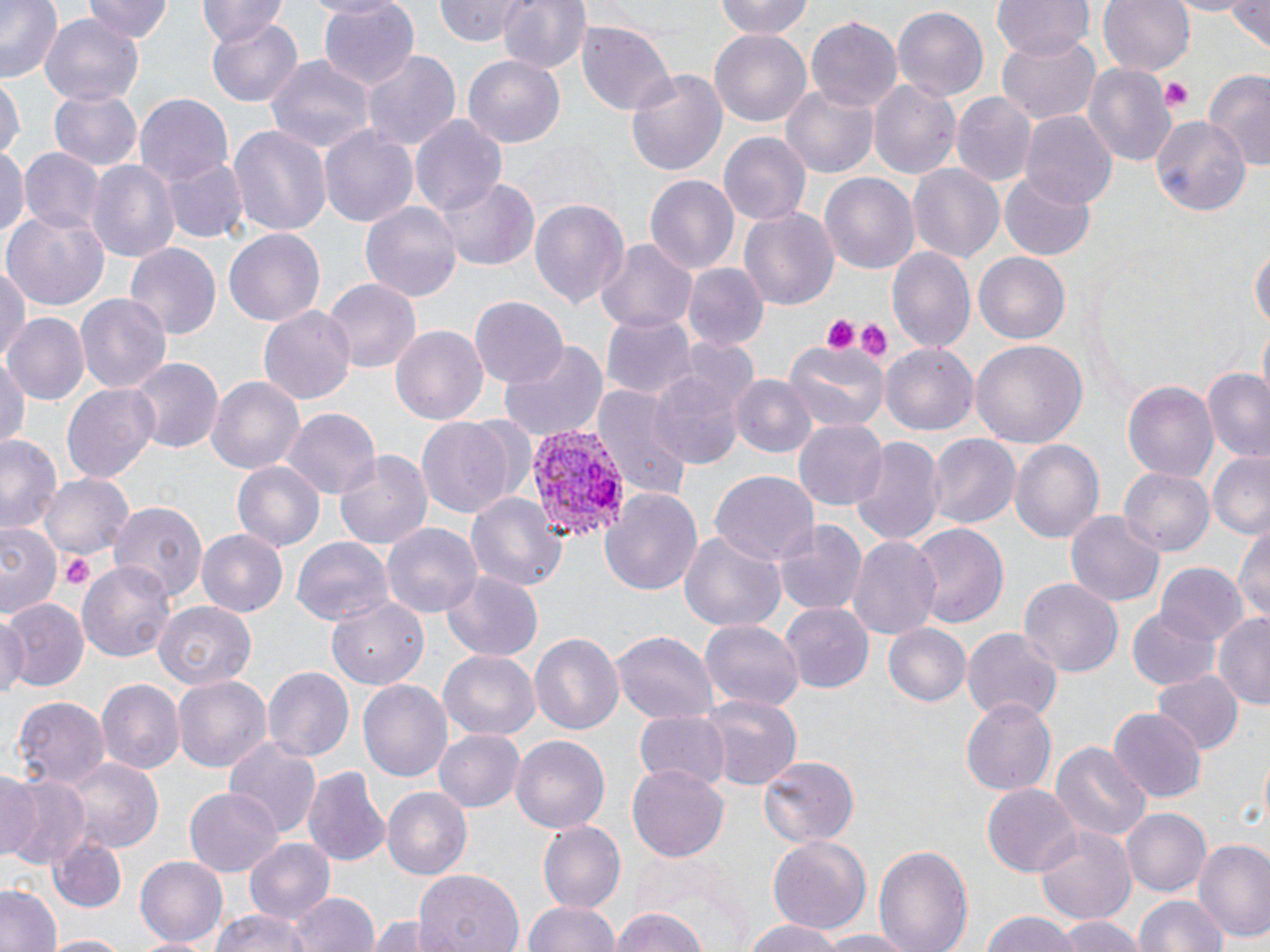

slide_level_diagnosis: Plasmodium vivax
uninfected_red_blood_cell_locations: 'approximate bounding boxes as (x1,y1)-(x2,y2) corner pairs in pixels: (0,0)-(64,80), (82,0)-(172,43), (198,0)-(289,46), (316,0)-(421,91), (496,0)-(591,76), (710,0)-(818,41), (992,0)-(1094,60), (1098,0)-(1196,80), (1166,0)-(1252,18), (1228,0)-(1269,50), (433,1)-(533,45), (893,5)-(989,101), (39,13)-(142,109), (804,14)-(901,112), (204,17)-(304,104), (577,21)-(675,114), (709,29)-(813,124), (995,30)-(1101,128), (361,50)-(461,149), (266,55)-(373,153), (463,55)-(565,150), (624,65)-(728,180), (1084,65)-(1175,167), (1205,71)-(1270,173), (868,77)-(960,180), (0,79)-(23,166), (781,84)-(879,178), (49,87)-(145,170), (949,92)-(1038,188), (134,93)-(234,188), (1021,111)-(1117,208), (411,115)-(508,219), (1149,116)-(1249,217), (226,125)-(332,237), (319,125)-(419,229), (719,131)-(810,226), (0,145)-(27,243), (18,148)-(101,234), (163,155)-(247,243), (86,158)-(179,264), (908,163)-(1004,263), (999,169)-(1098,259), (819,173)-(919,276), (644,174)-(739,274), (435,175)-(539,271), (529,196)-(629,311), (359,198)-(464,304), (739,206)-(839,310), (4,211)-(107,309), (224,228)-(324,324), (595,238)-(698,335), (1251,241)-(1269,341), (124,243)-(220,343), (887,245)-(975,355), (974,252)-(1070,345), (0,261)-(29,367), (683,263)-(766,350), (323,278)-(421,373), (73,293)-(171,394), (469,297)-(568,389), (260,305)-(355,404), (5,312)-(89,405), (601,312)-(694,401), (390,325)-(488,427), (498,341)-(608,441), (783,341)-(889,431), (970,341)-(1087,451), (881,344)-(978,437), (0,350)-(28,455), (127,356)-(223,454), (647,367)-(748,469), (1200,370)-(1270,463), (204,374)-(306,475), (731,376)-(814,458), (1122,380)-(1220,483), (62,384)-(162,482), (593,384)-(692,502), (285,409)-(379,502), (416,416)-(516,520), (794,417)-(889,511), (0,431)-(64,539), (849,434)-(945,548), (928,434)-(1020,532), (1009,438)-(1104,545), (335,448)-(434,551), (1206,452)-(1270,539), (231,459)-(324,550), (1118,467)-(1213,558), (40,473)-(134,563), (709,473)-(819,570), (600,486)-(704,597), (465,489)-(569,590), (109,499)-(207,606), (1063,509)-(1165,609), (770,518)-(867,618), (1233,518)-(1270,625), (908,520)-(1009,627), (1,523)-(61,617), (382,523)-(483,618), (198,528)-(288,616), (678,530)-(785,636), (846,533)-(942,640), (291,537)-(395,626), (78,560)-(179,663), (1154,562)-(1248,645), (441,571)-(542,661), (1019,578)-(1123,679), (328,596)-(431,687), (0,601)-(88,692), (155,601)-(256,691), (780,602)-(875,692), (1128,608)-(1220,690), (1214,613)-(1270,712), (0,615)-(26,705), (700,616)-(804,711), (883,622)-(971,707), (961,626)-(1062,723), (611,629)-(719,724), (528,632)-(624,736), (438,650)-(540,740), (262,664)-(354,761), (1151,671)-(1242,756), (171,675)-(271,772), (357,677)-(451,782), (97,680)-(183,775), (698,694)-(802,792), (11,696)-(112,788), (959,696)-(1057,795), (1109,707)-(1207,802), (632,709)-(732,791), (435,728)-(527,814), (509,734)-(611,835), (225,739)-(322,835), (1050,740)-(1151,846), (758,757)-(859,847), (69,759)-(163,852), (301,763)-(390,868), (628,763)-(726,862), (2,768)-(38,859), (0,770)-(86,870), (983,783)-(1082,876), (382,785)-(471,880), (185,787)-(281,877), (1122,808)-(1211,897), (536,821)-(625,915), (1035,823)-(1137,925), (766,836)-(870,937), (46,837)-(124,914), (245,838)-(335,925), (1192,838)-(1270,944), (872,841)-(973,952), (135,856)-(228,947), (414,870)-(523,952), (0,882)-(63,952), (292,891)-(378,952), (1136,894)-(1229,952), (523,900)-(623,952), (209,908)-(316,952), (609,910)-(709,951), (981,911)-(1084,952), (1057,914)-(1145,952), (369,916)-(439,951), (738,919)-(853,952), (807,931)-(922,952), (40,933)-(138,952)'
image_size: 1270×952 pixels
platelet_locations: 'approximate bounding boxes as (x1,y1)-(x2,y2) corner pairs in pixels: (1162,81)-(1193,109), (820,316)-(860,354), (852,319)-(894,360), (62,553)-(93,590)'
stain: May-Grünwald-Giemsa
modality: light microscopy
magnification: 1000x
plasmodium_vivax_infected_red_blood_cell_locations: 'approximate bounding boxes as (x1,y1)-(x2,y2) corner pairs in pixels: (522,421)-(629,541)'
field_of_view: one of a larger specimen
preparation: thin blood film